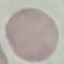
Result: no malaria parasites seen. Cell patch, automatically extracted from a larger field of view and resized to 64 × 64 pixels. Giemsa stain. Thin smear of blood. Acquired by smartphone through the microscope eyepiece.